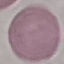
Result: no malaria parasites detected. Acquired by smartphone through the microscope eyepiece. Giemsa-stained preparation. Automatically extracted cell patch, resized to 64 × 64 pixels. Thin smear of blood.